Name the cell type shown.
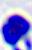
This is a leukocyte.

magnification = 400x
modality = photomicrograph